Identify the parasite.
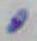
This is Toxoplasma gondii.

Captured at 1000x magnification. Micrograph.